Locate and identify every blood parasite.
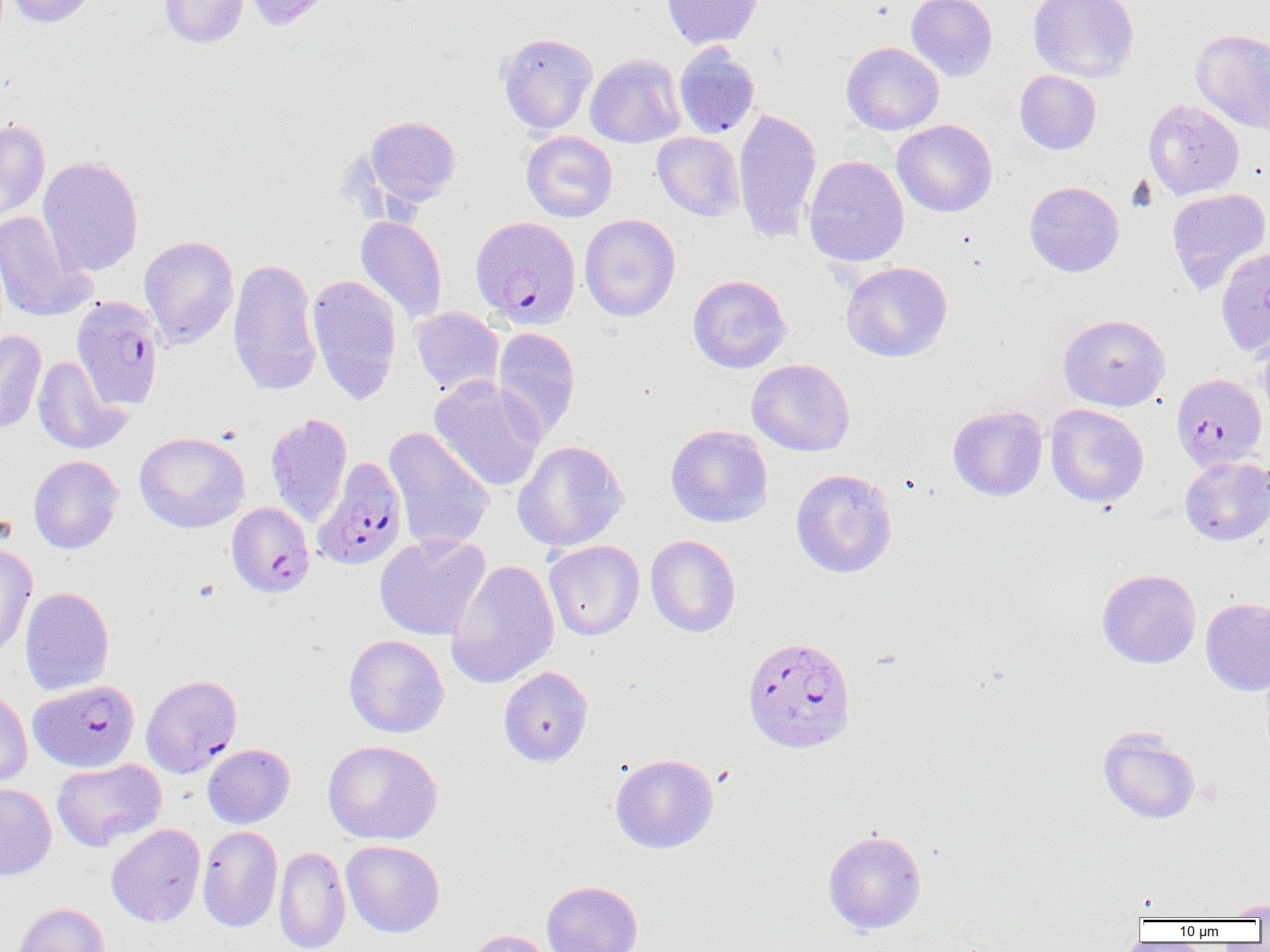

Approximate bounding boxes as named x1/y1/x2/y2 corners in pixels.
Plasmodium falciparum-infected red blood cells: (x1=471, y1=216, x2=581, y2=328), (x1=72, y1=296, x2=164, y2=409), (x1=1171, y1=373, x2=1267, y2=472), (x1=313, y1=457, x2=408, y2=570), (x1=225, y1=497, x2=313, y2=593), (x1=742, y1=636, x2=856, y2=753), (x1=141, y1=674, x2=242, y2=777), (x1=29, y1=680, x2=139, y2=772).
No Plasmodium ovale, Plasmodium malariae, Plasmodium vivax, Babesia divergens, or Trypanosoma brucei observed.

Uninfected red blood cell locations: (x1=7, y1=0, x2=98, y2=27), (x1=159, y1=0, x2=248, y2=48), (x1=243, y1=0, x2=337, y2=30), (x1=662, y1=0, x2=763, y2=49), (x1=906, y1=0, x2=998, y2=81), (x1=1028, y1=0, x2=1139, y2=82), (x1=1191, y1=28, x2=1270, y2=134), (x1=496, y1=32, x2=598, y2=134), (x1=841, y1=41, x2=944, y2=135), (x1=674, y1=45, x2=760, y2=138), (x1=585, y1=54, x2=685, y2=147), (x1=1015, y1=70, x2=1101, y2=154), (x1=1143, y1=99, x2=1245, y2=199), (x1=733, y1=107, x2=822, y2=244), (x1=363, y1=116, x2=461, y2=208), (x1=0, y1=119, x2=50, y2=222), (x1=892, y1=119, x2=997, y2=217), (x1=522, y1=131, x2=618, y2=222), (x1=652, y1=132, x2=745, y2=221), (x1=803, y1=155, x2=909, y2=267), (x1=38, y1=156, x2=143, y2=276), (x1=1025, y1=181, x2=1124, y2=277), (x1=1166, y1=187, x2=1270, y2=293), (x1=0, y1=210, x2=95, y2=322), (x1=579, y1=214, x2=681, y2=321), (x1=355, y1=216, x2=447, y2=325), (x1=139, y1=236, x2=239, y2=349), (x1=1215, y1=246, x2=1270, y2=357), (x1=228, y1=258, x2=322, y2=397), (x1=841, y1=261, x2=953, y2=363), (x1=307, y1=274, x2=402, y2=404), (x1=687, y1=274, x2=792, y2=373), (x1=410, y1=307, x2=504, y2=396), (x1=1058, y1=314, x2=1170, y2=411), (x1=492, y1=328, x2=581, y2=442), (x1=0, y1=330, x2=46, y2=434), (x1=1257, y1=330, x2=1270, y2=425), (x1=32, y1=355, x2=129, y2=455), (x1=746, y1=358, x2=855, y2=456), (x1=429, y1=376, x2=546, y2=492), (x1=1045, y1=404, x2=1148, y2=507), (x1=948, y1=405, x2=1047, y2=501), (x1=265, y1=413, x2=353, y2=527), (x1=665, y1=425, x2=773, y2=528), (x1=384, y1=427, x2=494, y2=552), (x1=134, y1=431, x2=250, y2=533), (x1=512, y1=440, x2=629, y2=551), (x1=28, y1=454, x2=124, y2=554), (x1=1180, y1=456, x2=1270, y2=546), (x1=790, y1=468, x2=897, y2=578), (x1=375, y1=533, x2=491, y2=641), (x1=646, y1=535, x2=741, y2=637), (x1=543, y1=540, x2=644, y2=640), (x1=0, y1=542, x2=37, y2=657), (x1=446, y1=560, x2=560, y2=689), (x1=1097, y1=569, x2=1201, y2=668), (x1=19, y1=586, x2=114, y2=696), (x1=1201, y1=597, x2=1270, y2=696), (x1=343, y1=634, x2=449, y2=738), (x1=499, y1=666, x2=593, y2=767), (x1=0, y1=686, x2=32, y2=787), (x1=1098, y1=728, x2=1201, y2=824), (x1=323, y1=740, x2=443, y2=845), (x1=202, y1=744, x2=295, y2=828), (x1=610, y1=753, x2=718, y2=853), (x1=52, y1=758, x2=166, y2=851), (x1=0, y1=783, x2=56, y2=880), (x1=106, y1=823, x2=206, y2=927), (x1=198, y1=825, x2=282, y2=932), (x1=823, y1=830, x2=926, y2=934), (x1=341, y1=839, x2=444, y2=937), (x1=274, y1=845, x2=351, y2=952), (x1=542, y1=880, x2=643, y2=952), (x1=1219, y1=899, x2=1270, y2=919), (x1=13, y1=902, x2=109, y2=952), (x1=463, y1=930, x2=557, y2=952). Slide-level diagnosis: Plasmodium falciparum. Image is 1270×952 pixels. Thin blood film. Light microscopy. Single field of view. 1000x magnification.